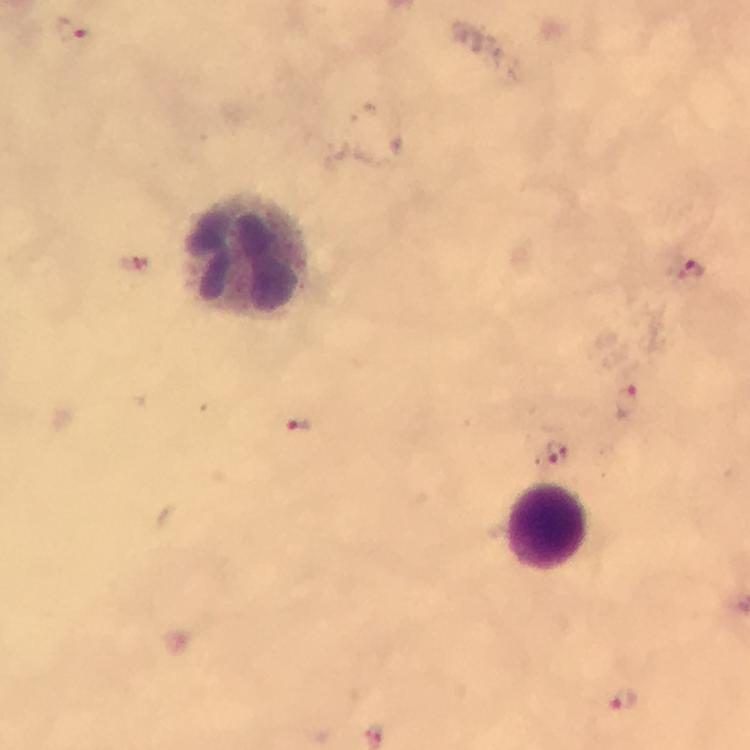

context = from a diagnostic examination for malaria
capture = smartphone photograph through a microscope
magnification = 100x
leukocyte locations = approximate centers as {x, y} in pixels: {247, 252}, {547, 527}
preparation = thick smear
cropped from = a single field of view
immersion oil = applied
stain = Giemsa
image size = 750×750 pixels
Plasmodium parasite locations = approximate centers as {x, y} in pixels: {68, 31}, {690, 271}, {627, 404}, {298, 425}, {556, 454}, {623, 700}